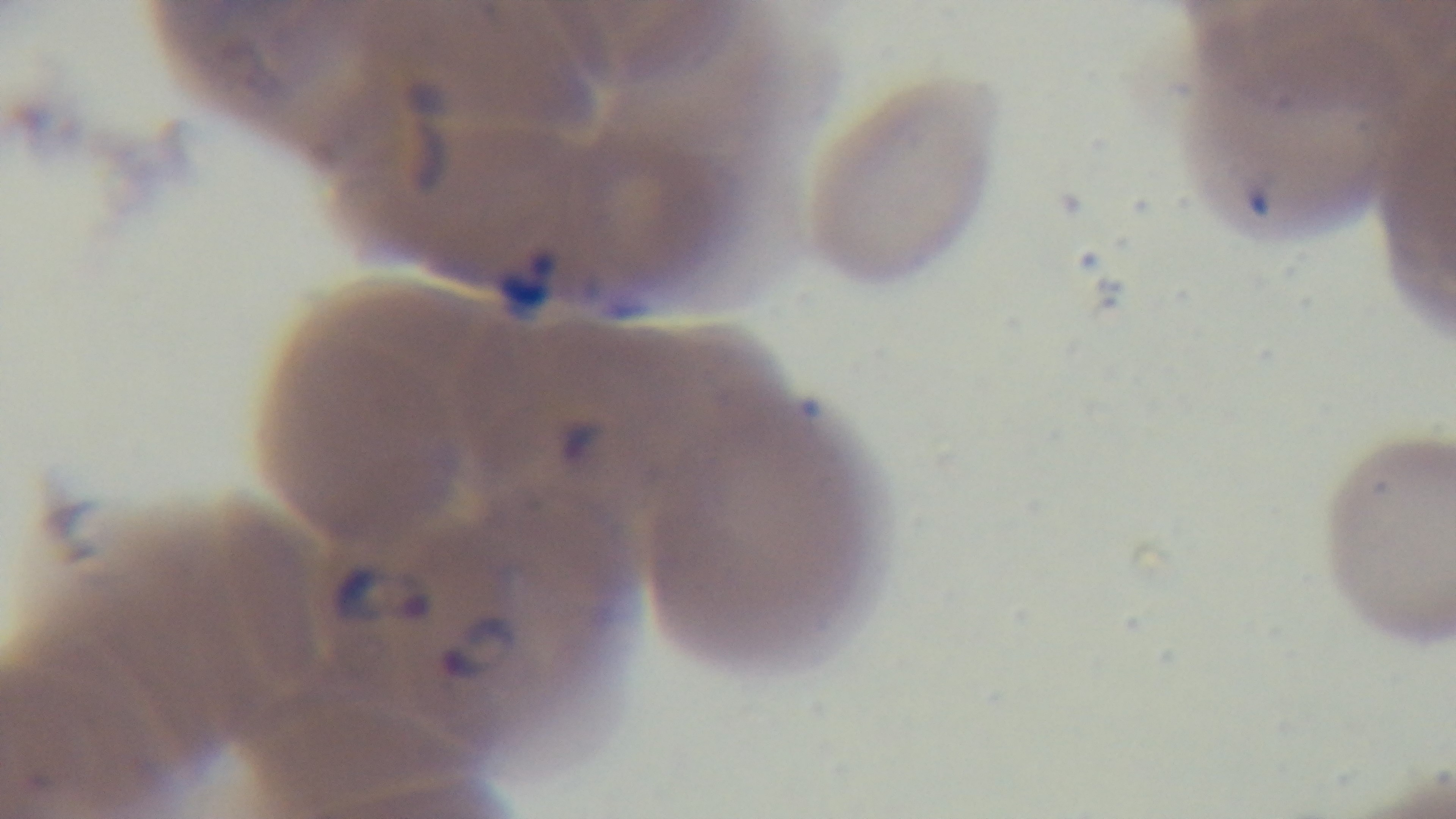
preparation: thin blood film
objective: 100x oil immersion
malaria_status: infected
stain: Giemsa
modality: light microscopy
capture: mounted 4K digital camera
field_of_view: single